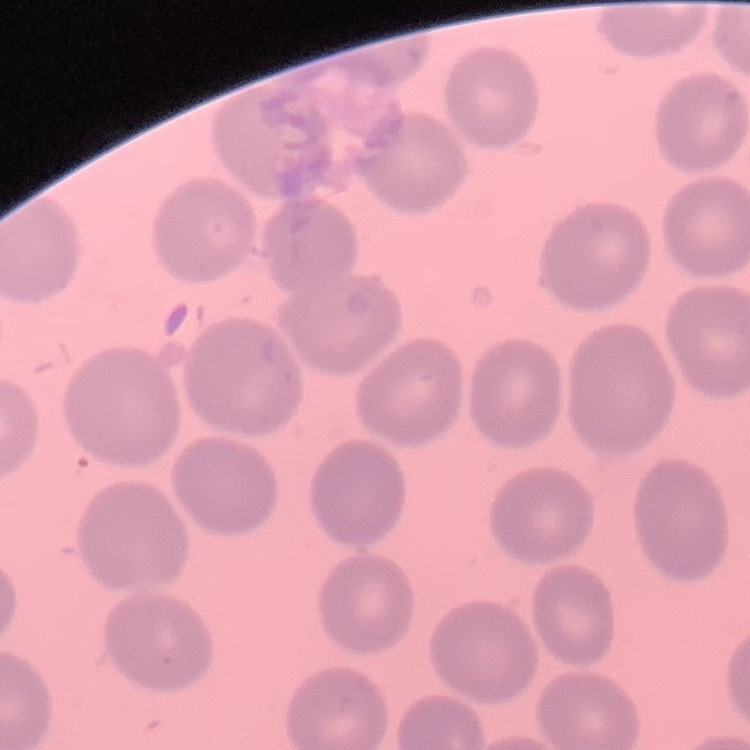
Summary:
  - Erythrocyte morphology: no rouleaux formation
  - Preparation: thin blood smear
  - Image type: one tile cut from a larger photomicrograph
  - Stain: Field's or Giemsa